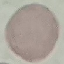
result = no malaria parasites detected
stain = Giemsa
capture = smartphone through the microscope eyepiece
preparation = thin blood smear
image type = automatically extracted cell patch, resized to 64 × 64 pixels